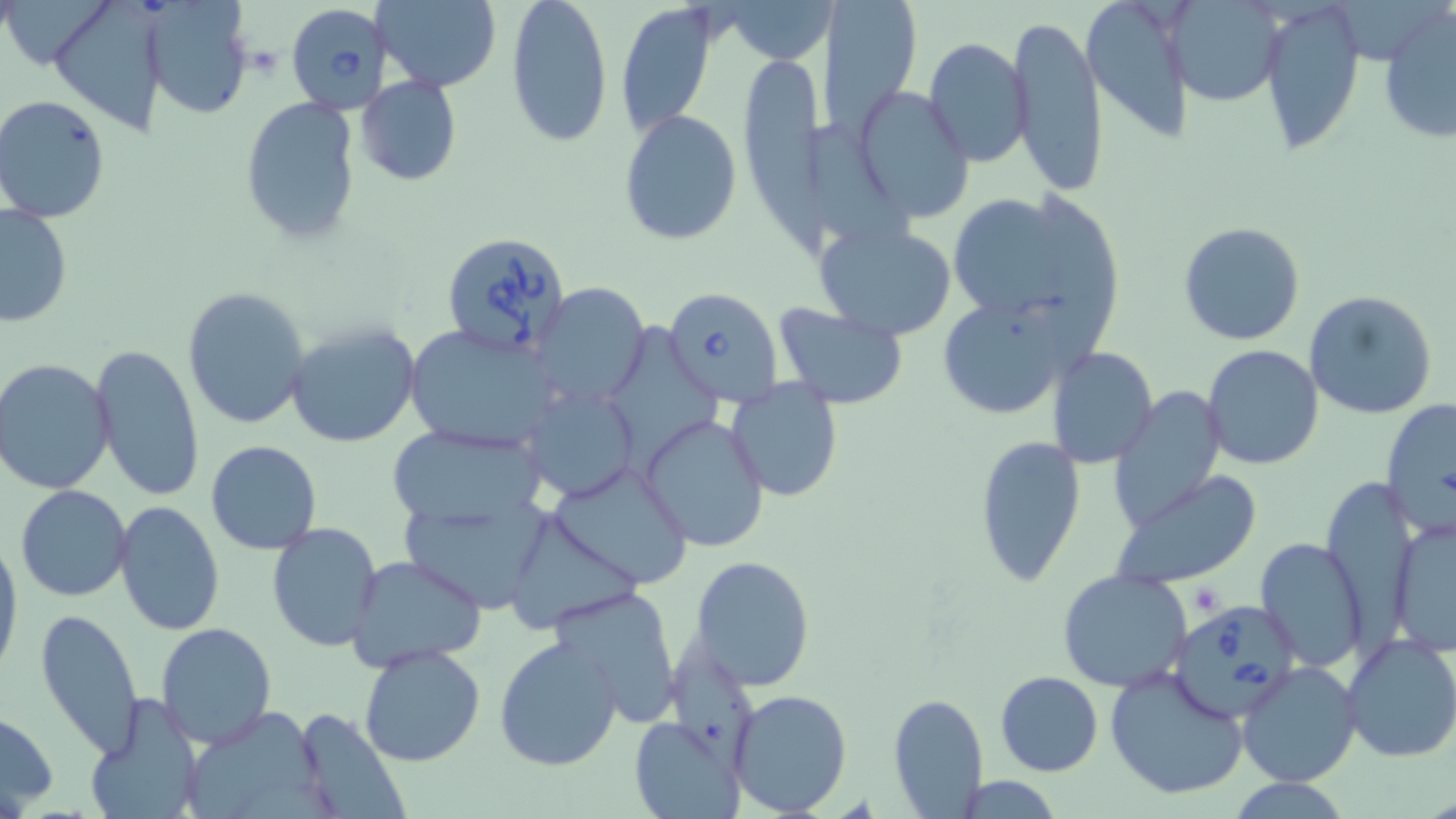

Approximate bounding boxes as named x1/y1/x2/y2 corners in pixels. Platelet locations: (x1=1186, y1=581, x2=1228, y2=615). Uninfected red blood cell locations: (x1=3, y1=0, x2=119, y2=68), (x1=47, y1=0, x2=173, y2=134), (x1=140, y1=0, x2=254, y2=119), (x1=505, y1=0, x2=614, y2=147), (x1=820, y1=0, x2=923, y2=137), (x1=1080, y1=0, x2=1195, y2=141), (x1=1259, y1=0, x2=1365, y2=157), (x1=372, y1=1, x2=504, y2=90), (x1=1167, y1=1, x2=1287, y2=106), (x1=730, y1=2, x2=830, y2=61), (x1=616, y1=3, x2=717, y2=137), (x1=1378, y1=4, x2=1456, y2=145), (x1=1008, y1=14, x2=1109, y2=195), (x1=922, y1=37, x2=1031, y2=168), (x1=733, y1=48, x2=844, y2=256), (x1=356, y1=75, x2=462, y2=187), (x1=857, y1=87, x2=975, y2=223), (x1=1, y1=94, x2=111, y2=222), (x1=238, y1=95, x2=363, y2=245), (x1=620, y1=108, x2=742, y2=247), (x1=803, y1=115, x2=917, y2=251), (x1=943, y1=192, x2=1118, y2=348), (x1=0, y1=204, x2=72, y2=329), (x1=1177, y1=220, x2=1306, y2=347), (x1=815, y1=221, x2=957, y2=339), (x1=533, y1=283, x2=650, y2=410), (x1=182, y1=287, x2=313, y2=431), (x1=935, y1=289, x2=1089, y2=422), (x1=1302, y1=290, x2=1437, y2=420), (x1=773, y1=304, x2=910, y2=408), (x1=284, y1=319, x2=420, y2=448), (x1=605, y1=322, x2=719, y2=475), (x1=404, y1=324, x2=564, y2=452), (x1=89, y1=342, x2=205, y2=502), (x1=1204, y1=345, x2=1324, y2=469), (x1=1048, y1=347, x2=1158, y2=467), (x1=0, y1=359, x2=115, y2=495), (x1=726, y1=380, x2=846, y2=502), (x1=519, y1=386, x2=638, y2=501), (x1=1110, y1=387, x2=1227, y2=528), (x1=1382, y1=399, x2=1455, y2=533), (x1=640, y1=413, x2=770, y2=553), (x1=384, y1=421, x2=548, y2=535), (x1=974, y1=433, x2=1086, y2=587), (x1=205, y1=440, x2=323, y2=554), (x1=544, y1=463, x2=694, y2=589), (x1=1109, y1=473, x2=1261, y2=591), (x1=16, y1=485, x2=131, y2=601), (x1=401, y1=496, x2=562, y2=609), (x1=115, y1=502, x2=225, y2=635), (x1=506, y1=507, x2=645, y2=632), (x1=1387, y1=516, x2=1455, y2=657), (x1=264, y1=521, x2=383, y2=652), (x1=0, y1=533, x2=22, y2=682), (x1=1253, y1=538, x2=1368, y2=672), (x1=345, y1=555, x2=487, y2=674), (x1=690, y1=556, x2=816, y2=691), (x1=1057, y1=569, x2=1194, y2=695), (x1=546, y1=585, x2=685, y2=724), (x1=35, y1=608, x2=145, y2=756), (x1=155, y1=622, x2=277, y2=748), (x1=669, y1=631, x2=754, y2=780), (x1=1341, y1=634, x2=1456, y2=763), (x1=494, y1=635, x2=625, y2=772), (x1=358, y1=644, x2=486, y2=768), (x1=1237, y1=662, x2=1363, y2=787), (x1=1103, y1=663, x2=1250, y2=800), (x1=995, y1=671, x2=1104, y2=776), (x1=730, y1=688, x2=853, y2=816), (x1=887, y1=692, x2=988, y2=818), (x1=82, y1=693, x2=204, y2=819), (x1=0, y1=706, x2=60, y2=813), (x1=176, y1=706, x2=335, y2=819), (x1=289, y1=706, x2=412, y2=819), (x1=628, y1=716, x2=744, y2=819), (x1=947, y1=775, x2=1070, y2=817), (x1=1225, y1=777, x2=1356, y2=817). Babesia divergens-infected red blood cell locations: (x1=287, y1=4, x2=393, y2=123), (x1=440, y1=229, x2=573, y2=362), (x1=662, y1=287, x2=782, y2=406), (x1=1166, y1=604, x2=1317, y2=733). Slide-level diagnosis: Babesia divergens. 1000x magnification. Thin blood film. Image is 1456×819 pixels. Single field of view. Light microscopy. May-Grünwald-Giemsa-stained preparation.